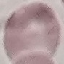
result = no malaria parasites detected
stain = Giemsa
capture = smartphone camera at the microscope eyepiece
image type = cell patch, automatically extracted from a larger field of view and resized to 64 × 64 pixels
preparation = thin smear